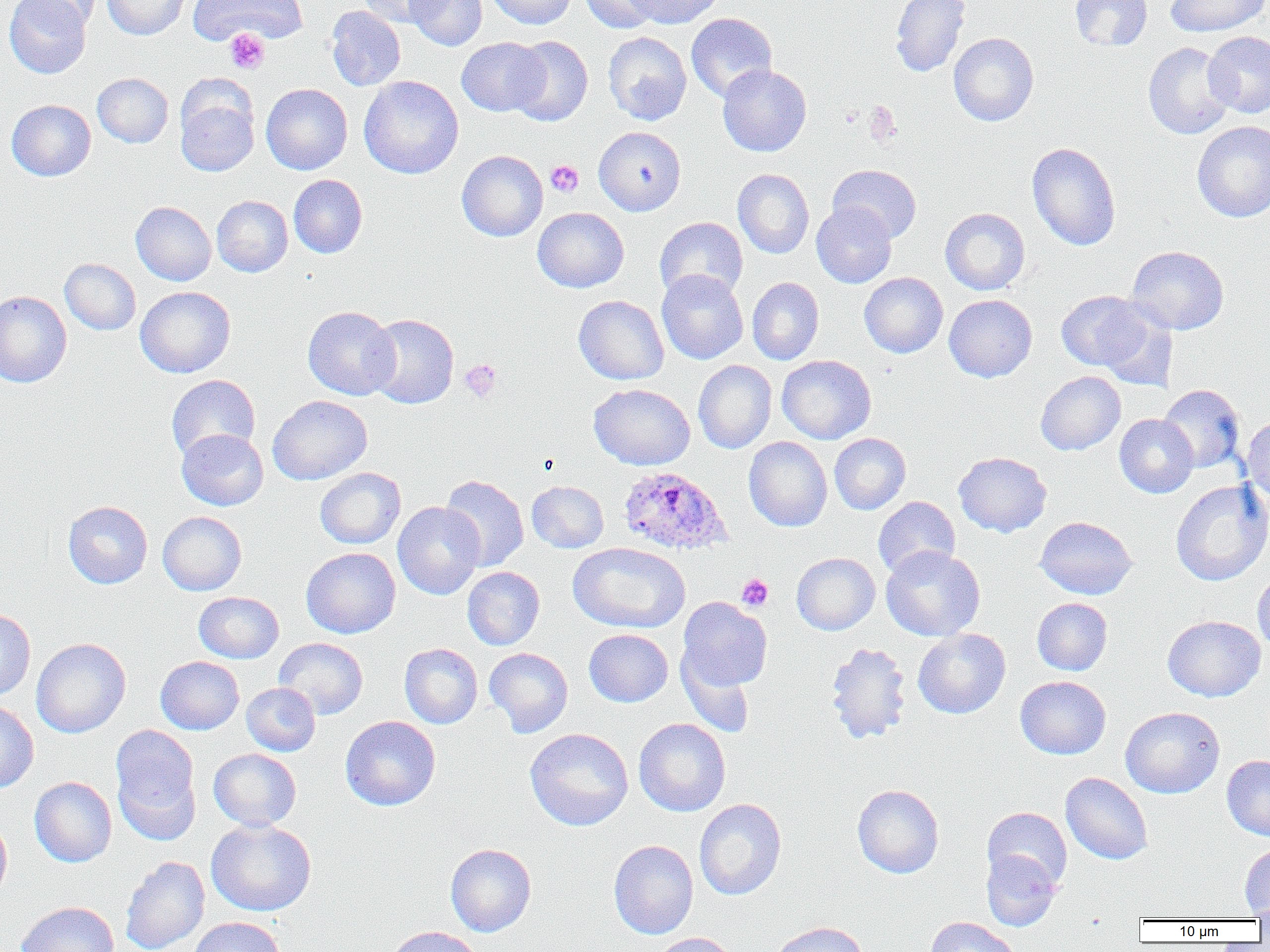
Approximate bounding boxes as (x1, y1, x2, y2) in pixels. Platelet locations: (224, 29, 270, 74), (546, 160, 583, 197), (460, 359, 502, 402), (736, 574, 774, 611). Uninfected red blood cell locations: (4, 0, 92, 78), (14, 0, 102, 31), (102, 0, 191, 40), (187, 0, 308, 46), (359, 0, 447, 27), (405, 0, 487, 51), (486, 0, 576, 30), (580, 0, 660, 34), (627, 0, 723, 28), (890, 0, 970, 78), (1070, 0, 1152, 51), (1166, 0, 1267, 37), (326, 6, 405, 91), (686, 13, 777, 103), (1203, 31, 1270, 118), (603, 32, 691, 125), (948, 33, 1038, 126), (508, 36, 593, 126), (457, 37, 549, 116), (1143, 42, 1235, 140), (718, 64, 812, 157), (92, 73, 173, 147), (359, 75, 463, 179), (261, 83, 352, 174), (175, 90, 259, 177), (6, 99, 96, 181), (1192, 121, 1270, 222), (594, 126, 686, 215), (1027, 142, 1121, 251), (457, 150, 548, 241), (828, 164, 922, 243), (733, 168, 814, 258), (289, 174, 367, 258), (212, 196, 293, 277), (131, 201, 216, 285), (811, 201, 897, 288), (533, 207, 629, 292), (940, 208, 1030, 295), (654, 217, 748, 302), (1127, 246, 1229, 334), (60, 258, 141, 335), (656, 270, 748, 364), (859, 272, 948, 358), (747, 277, 824, 365), (135, 286, 236, 377), (0, 290, 72, 388), (1056, 290, 1154, 371), (944, 294, 1037, 382), (573, 295, 669, 384), (302, 306, 400, 400), (1095, 306, 1178, 391), (366, 313, 459, 409), (777, 355, 876, 444), (693, 360, 776, 454), (1035, 371, 1125, 455), (166, 374, 260, 462), (589, 383, 695, 470), (1158, 384, 1245, 472), (267, 395, 372, 485), (1114, 413, 1198, 498), (1242, 416, 1270, 507), (176, 429, 268, 510), (830, 433, 911, 514), (743, 436, 832, 532), (953, 452, 1052, 537), (315, 467, 405, 549), (440, 475, 529, 571), (1170, 479, 1270, 586), (526, 480, 609, 553), (873, 496, 960, 578), (62, 501, 152, 588), (393, 501, 486, 600), (158, 511, 246, 595), (1035, 516, 1137, 600), (568, 542, 690, 633), (881, 546, 985, 641), (301, 547, 400, 638), (792, 553, 880, 635), (462, 567, 545, 650), (1252, 568, 1270, 656), (194, 591, 284, 663), (677, 597, 772, 693), (1032, 597, 1112, 675), (0, 609, 36, 700), (1162, 615, 1266, 702), (912, 628, 1011, 718), (584, 629, 673, 707), (274, 637, 368, 719), (31, 638, 131, 738), (825, 642, 912, 744), (400, 643, 483, 728), (484, 647, 573, 737), (677, 650, 757, 736), (156, 656, 244, 734), (1015, 676, 1111, 759), (241, 683, 320, 756), (0, 698, 38, 793), (1120, 706, 1225, 798), (340, 716, 441, 811), (633, 718, 730, 817), (109, 725, 201, 843), (525, 728, 633, 830), (209, 748, 301, 830), (1221, 755, 1270, 840), (1061, 772, 1153, 865), (29, 776, 117, 867), (852, 784, 944, 878), (694, 798, 786, 900), (982, 807, 1072, 891), (0, 814, 12, 905), (206, 818, 316, 916), (608, 839, 698, 939), (445, 843, 536, 936), (1240, 843, 1270, 918), (981, 850, 1060, 931), (120, 856, 210, 952), (16, 901, 119, 952), (1250, 901, 1270, 927), (925, 916, 1021, 952), (190, 917, 284, 952), (769, 921, 870, 952), (386, 925, 483, 952), (650, 933, 739, 952). Plasmodium ovale-infected red blood cell locations: (619, 466, 731, 555). Slide-level diagnosis: Plasmodium ovale. One field of a larger specimen. Light microscopy. Captured at 1000x magnification. Image is 1270×952 pixels. Thin blood smear.